Identify the parasite.
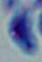
Toxoplasma gondii.

1000x magnification. Micrograph.